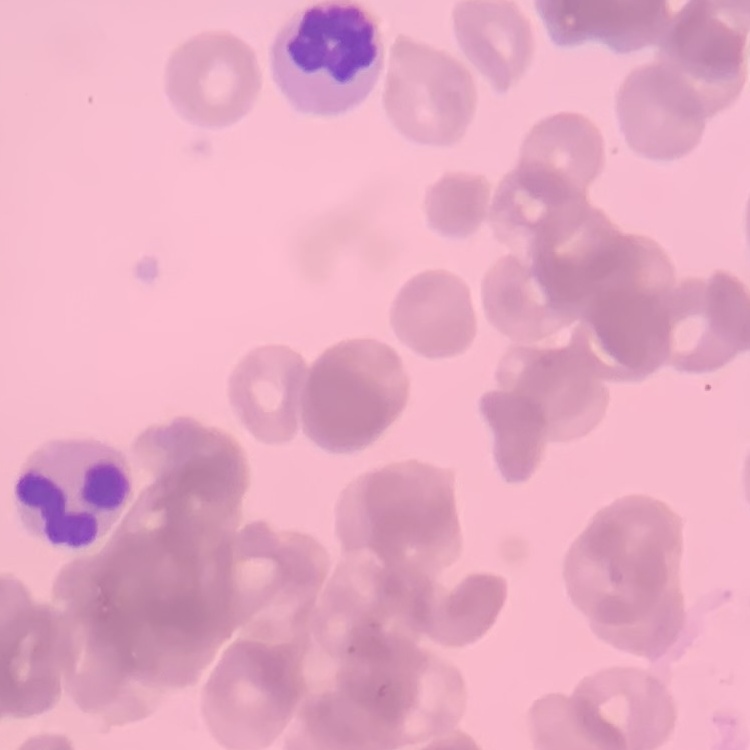

erythrocyte morphology = rouleaux formation
image type = one tile cut from a larger photomicrograph
preparation = thin blood film
stain = Field's or Giemsa